Assess this cell for malaria.
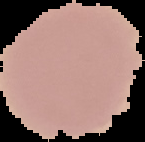
Uninfected.

image size = 145×142 pixels
image type = segmented cell region on a black background
preparation = thin blood film